Identify the parasite.
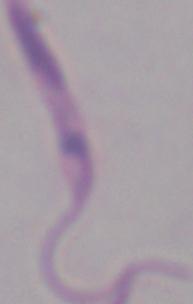
This is Leishmania.

modality: micrograph
magnification: 1000x